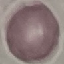

Summary:
  - Malaria status: uninfected
  - Image type: automatically extracted cell patch, resized to 64 × 64 pixels
  - Preparation: thin blood film
  - Capture: smartphone camera at the microscope eyepiece
  - Stain: Giemsa